Locate and identify every blood parasite.
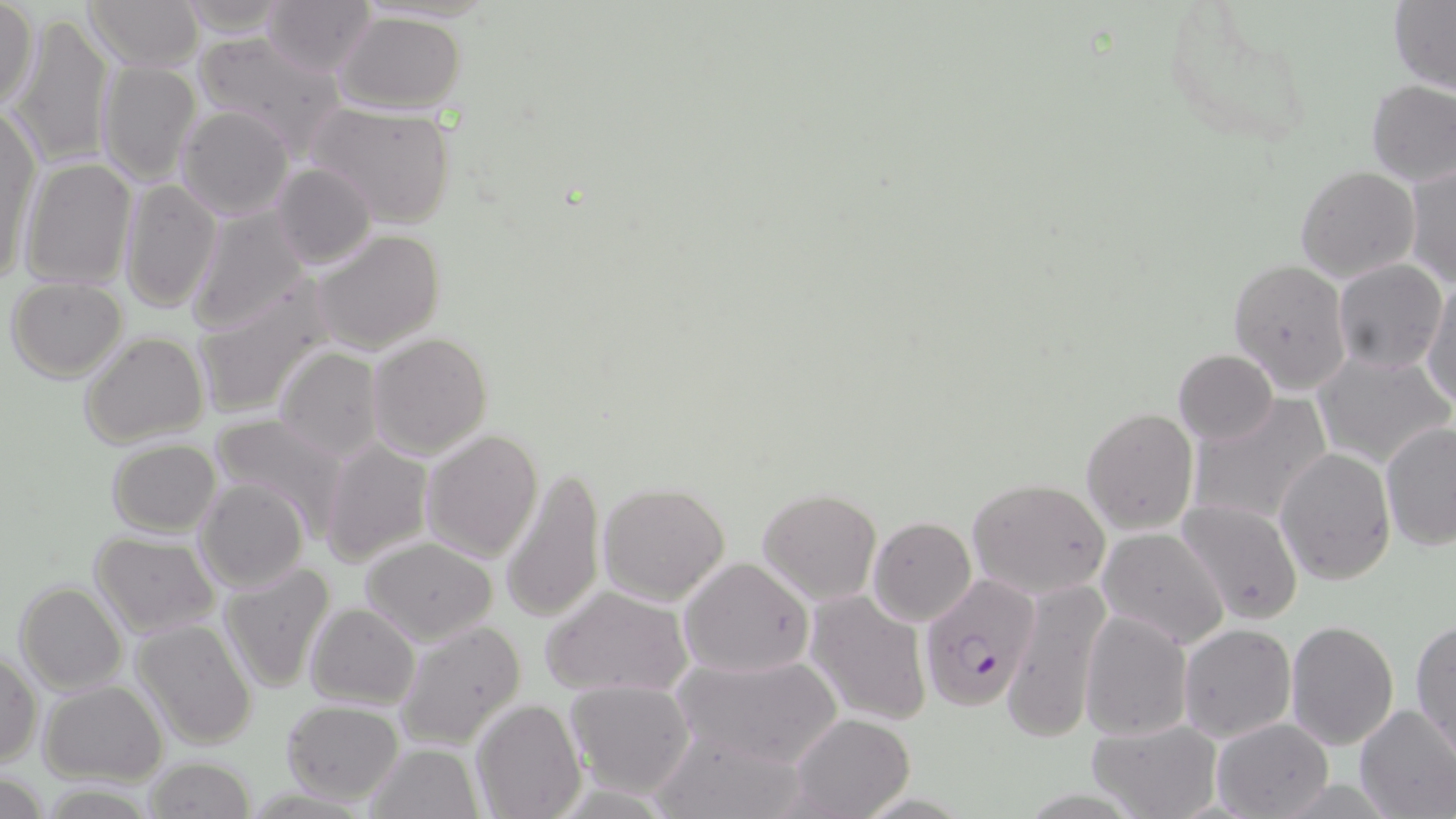

Approximate bounding boxes as named x1/y1/x2/y2 corners in pixels.
Plasmodium falciparum-infected red blood cells: (x1=920, y1=575, x2=1042, y2=709).
No Plasmodium ovale, Plasmodium malariae, Plasmodium vivax, Babesia divergens, or Trypanosoma brucei observed.

Uninfected red blood cell locations: (x1=0, y1=0, x2=40, y2=115), (x1=83, y1=0, x2=202, y2=71), (x1=171, y1=0, x2=293, y2=37), (x1=1390, y1=1, x2=1456, y2=94), (x1=263, y1=2, x2=377, y2=78), (x1=1166, y1=6, x2=1313, y2=152), (x1=334, y1=9, x2=468, y2=115), (x1=7, y1=13, x2=116, y2=169), (x1=192, y1=33, x2=344, y2=157), (x1=97, y1=60, x2=201, y2=185), (x1=1366, y1=80, x2=1456, y2=186), (x1=303, y1=101, x2=459, y2=228), (x1=175, y1=105, x2=294, y2=220), (x1=1, y1=111, x2=42, y2=286), (x1=21, y1=157, x2=137, y2=291), (x1=1404, y1=157, x2=1455, y2=291), (x1=272, y1=161, x2=376, y2=270), (x1=1295, y1=164, x2=1420, y2=282), (x1=119, y1=178, x2=221, y2=313), (x1=186, y1=206, x2=311, y2=335), (x1=313, y1=228, x2=444, y2=355), (x1=1331, y1=258, x2=1448, y2=373), (x1=1228, y1=259, x2=1352, y2=395), (x1=6, y1=277, x2=127, y2=382), (x1=192, y1=278, x2=340, y2=420), (x1=1420, y1=280, x2=1456, y2=408), (x1=78, y1=330, x2=210, y2=449), (x1=367, y1=332, x2=493, y2=459), (x1=1314, y1=345, x2=1454, y2=469), (x1=273, y1=347, x2=386, y2=462), (x1=1173, y1=349, x2=1278, y2=446), (x1=1186, y1=395, x2=1333, y2=531), (x1=1081, y1=406, x2=1198, y2=535), (x1=210, y1=411, x2=353, y2=541), (x1=1380, y1=420, x2=1456, y2=551), (x1=422, y1=429, x2=544, y2=561), (x1=319, y1=438, x2=433, y2=569), (x1=107, y1=439, x2=221, y2=535), (x1=1276, y1=445, x2=1396, y2=585), (x1=500, y1=465, x2=607, y2=624), (x1=194, y1=477, x2=308, y2=593), (x1=967, y1=478, x2=1111, y2=599), (x1=597, y1=481, x2=731, y2=603), (x1=757, y1=489, x2=881, y2=605), (x1=1176, y1=501, x2=1304, y2=626), (x1=162, y1=507, x2=297, y2=627), (x1=867, y1=516, x2=975, y2=626), (x1=1097, y1=525, x2=1231, y2=649), (x1=90, y1=531, x2=221, y2=637), (x1=359, y1=536, x2=498, y2=644), (x1=678, y1=557, x2=816, y2=678), (x1=220, y1=561, x2=337, y2=694), (x1=1002, y1=576, x2=1115, y2=741), (x1=14, y1=582, x2=126, y2=696), (x1=540, y1=584, x2=695, y2=699), (x1=806, y1=592, x2=932, y2=726), (x1=304, y1=603, x2=419, y2=711), (x1=1081, y1=612, x2=1190, y2=740), (x1=1410, y1=618, x2=1456, y2=760), (x1=131, y1=619, x2=258, y2=750), (x1=393, y1=620, x2=526, y2=751), (x1=1285, y1=620, x2=1400, y2=752), (x1=1177, y1=623, x2=1296, y2=743), (x1=673, y1=651, x2=842, y2=769), (x1=1, y1=652, x2=43, y2=767), (x1=564, y1=678, x2=696, y2=797), (x1=39, y1=681, x2=168, y2=784), (x1=470, y1=698, x2=587, y2=819), (x1=279, y1=699, x2=404, y2=804), (x1=1354, y1=704, x2=1456, y2=818), (x1=790, y1=714, x2=915, y2=819), (x1=1085, y1=717, x2=1223, y2=819), (x1=1209, y1=718, x2=1333, y2=819), (x1=652, y1=729, x2=808, y2=819), (x1=365, y1=741, x2=484, y2=818), (x1=142, y1=755, x2=256, y2=819), (x1=0, y1=770, x2=48, y2=817), (x1=38, y1=782, x2=161, y2=817). Slide-level diagnosis: Plasmodium falciparum. Thin blood smear. May-Grünwald-Giemsa stain. Captured at 1000x magnification. One field of a larger specimen. Image is 1456×819 pixels. Optical microscopy.